Describe the morphology of the erythrocytes.
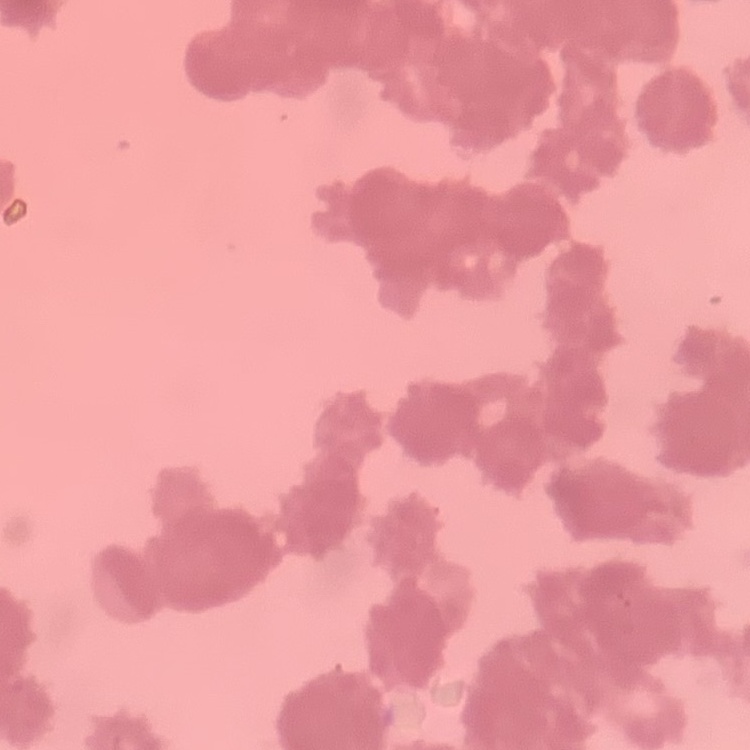

They show rouleaux formation.

image type = one tile cut from a larger photomicrograph
stain = Field's or Giemsa
preparation = thin blood film